State which parasite is depicted.
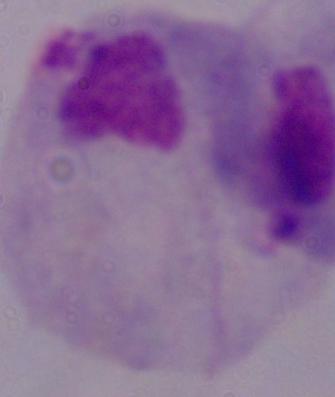

A trichomonad.

Summary:
  - Modality: photomicrograph
  - Magnification: 1000x